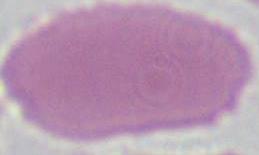
Summary:
  - Modality: photomicrograph
  - Identification: red blood cell
  - Magnification: 1000x